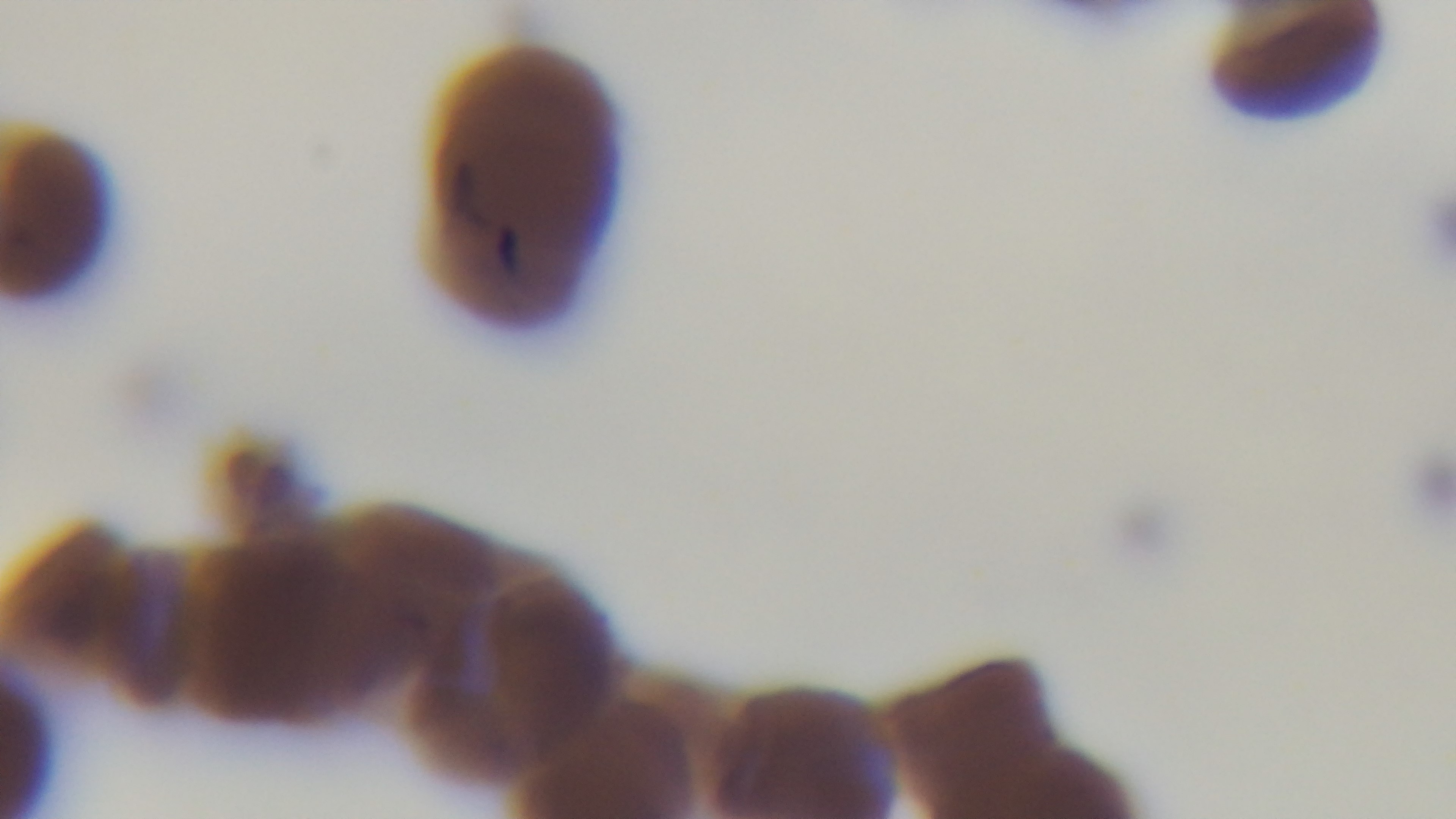

field_of_view: single
modality: light microscopy
capture: mounted 4K digital camera
malaria_status: positive
preparation: thin blood film
objective: 100x oil immersion
stain: Giemsa